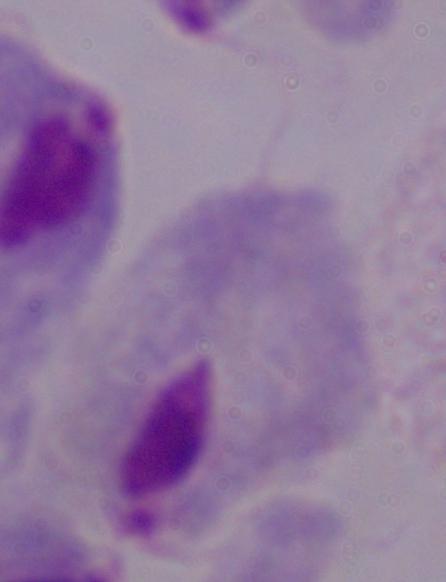 Captured at 1000x magnification. Micrograph. A trichomonad is shown.